Assess this cell for malaria.
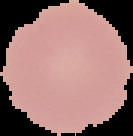
Uninfected.

preparation = thin blood smear
image size = 133×136 pixels
image type = segmented cell region with the area outside set to black